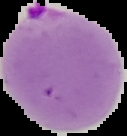
Summary:
  - Result: malaria parasites detected
  - Preparation: thin blood smear
  - Image type: cell region segmented out of the field of view; surrounding area masked to black
  - Image size: 127×136 pixels